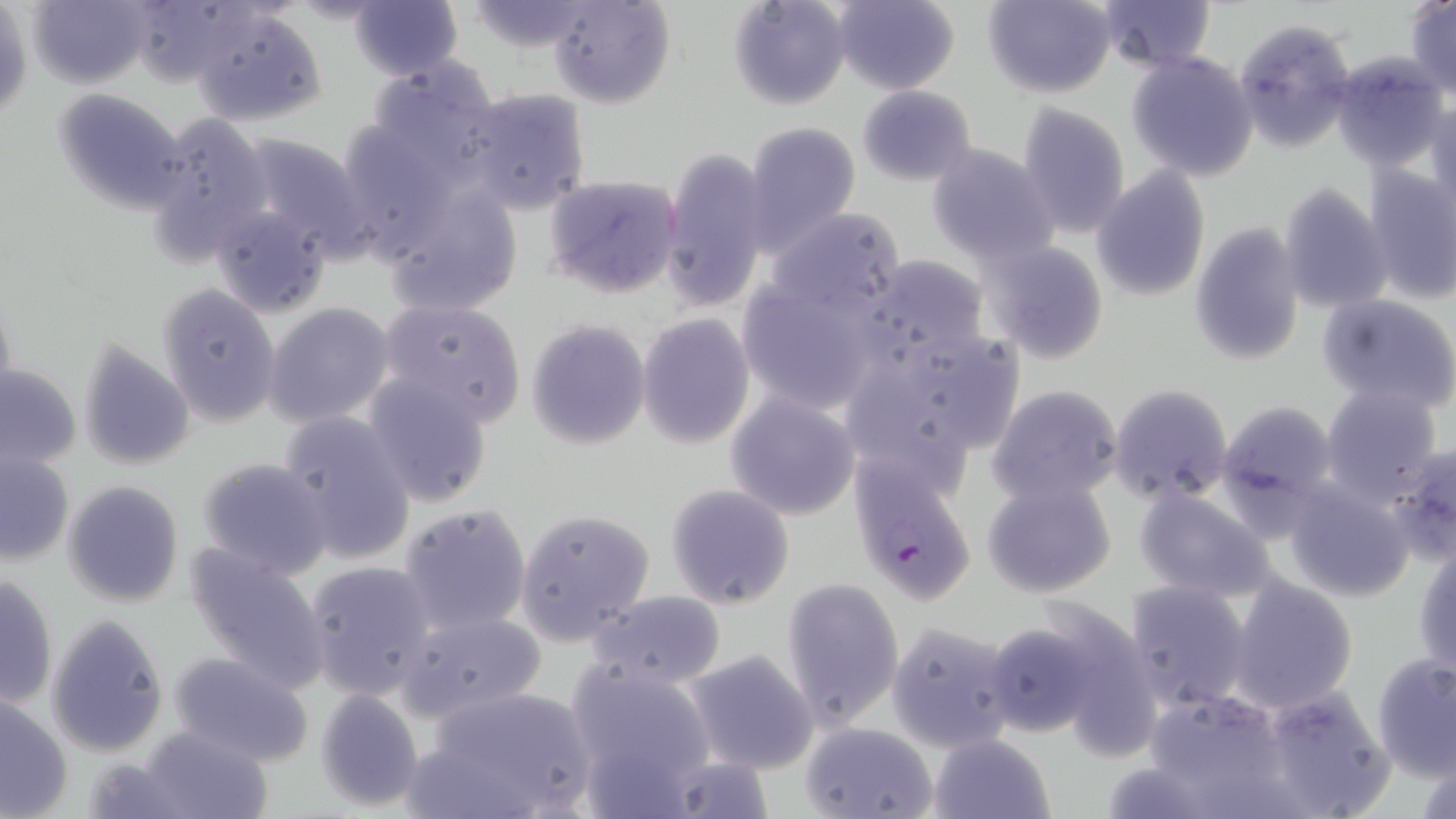
Summary:
  - Coordinate format: approximate bounding boxes as (x1, y1, x2, y2) in pixels
  - Plasmodium falciparum-infected red blood cell locations: (848, 454, 980, 604)
  - Uninfected red blood cell locations: (27, 0, 153, 88), (122, 0, 250, 85), (546, 0, 675, 108), (728, 0, 851, 109), (830, 0, 959, 93), (982, 0, 1119, 98), (462, 1, 602, 52), (1097, 1, 1217, 73), (1405, 1, 1456, 97), (350, 2, 461, 79), (192, 5, 328, 127), (1, 6, 30, 123), (1234, 17, 1356, 152), (1126, 50, 1259, 182), (1330, 51, 1452, 172), (360, 57, 507, 184), (856, 85, 978, 186), (465, 86, 592, 216), (52, 87, 190, 213), (1425, 99, 1456, 212), (1015, 101, 1131, 239), (145, 110, 275, 266), (743, 121, 863, 251), (232, 132, 372, 258), (925, 143, 1059, 267), (658, 144, 773, 313), (1363, 165, 1456, 306), (1093, 169, 1211, 301), (542, 173, 682, 299), (382, 174, 526, 317), (1276, 185, 1389, 312), (209, 201, 338, 320), (765, 208, 906, 319), (1189, 222, 1306, 365), (982, 240, 1109, 365), (852, 254, 993, 371), (735, 274, 885, 413), (157, 283, 282, 426), (1317, 292, 1456, 414), (379, 299, 527, 423), (264, 302, 396, 429), (637, 314, 755, 449), (526, 318, 651, 451), (837, 327, 1025, 485), (75, 339, 196, 472), (0, 363, 81, 470), (361, 370, 492, 508), (986, 383, 1126, 509), (1108, 383, 1235, 504), (1321, 386, 1441, 499), (725, 394, 861, 520), (1217, 399, 1339, 515), (278, 410, 416, 565), (1393, 439, 1456, 562), (0, 448, 74, 564), (195, 455, 335, 579), (1280, 474, 1421, 599), (980, 476, 1117, 600), (62, 479, 183, 607), (664, 483, 796, 610), (1134, 486, 1277, 602), (398, 503, 530, 633), (516, 507, 655, 644), (1414, 541, 1456, 675), (185, 544, 332, 689), (303, 559, 436, 699), (1, 571, 57, 711), (782, 576, 905, 728), (1228, 576, 1358, 712), (1123, 580, 1252, 710), (584, 589, 728, 690), (394, 610, 547, 722), (44, 613, 170, 757), (983, 619, 1107, 738), (887, 621, 1020, 752), (684, 650, 818, 774), (167, 651, 314, 767), (1371, 653, 1456, 779), (563, 659, 719, 799), (1258, 682, 1395, 817), (413, 686, 599, 819), (313, 688, 425, 813), (1147, 688, 1299, 815), (0, 694, 73, 818), (797, 719, 939, 819), (141, 725, 272, 819), (928, 733, 1057, 819), (82, 757, 189, 816)
  - Slide-level diagnosis: Plasmodium falciparum
  - Field of view: single
  - Modality: optical microscopy
  - Preparation: thin blood smear
  - Image size: 1456×819 pixels
  - Magnification: 1000x
  - Stain: May-Grünwald-Giemsa